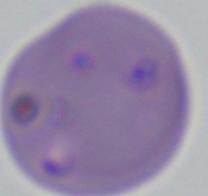

Micrograph. A Babesia parasite is seen. 1000x magnification.